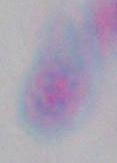

modality = photomicrograph
identification = Toxoplasma gondii
magnification = 1000x